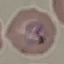

Summary:
  - Result: malaria parasites identified
  - Stain: Giemsa
  - Image type: cell patch, automatically extracted from a larger field of view and resized to 64 × 64 pixels
  - Capture: smartphone camera at the microscope eyepiece
  - Preparation: thin blood smear